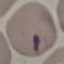

malaria status = parasitized
capture = smartphone camera at the microscope eyepiece
preparation = thin smear
stain = Giemsa
image type = cell patch, automatically extracted from a larger field of view and resized to 64 × 64 pixels